Classify this cell by malaria status.
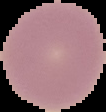

Uninfected.

{
  "image_type": "segmented cell region on a black background",
  "image_size": "106×112 pixels",
  "preparation": "thin blood film"
}